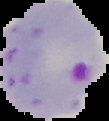
Image is 109×121 pixels. From a thin blood film. Segmented cell region on a black background. Result: Plasmodium parasites identified.